Report the malaria status of this cell.
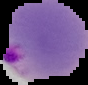
Parasitized.

preparation = thin blood smear
image size = 88×85 pixels
image type = segmented cell region on a black background